Assess the morphology of the erythrocytes.
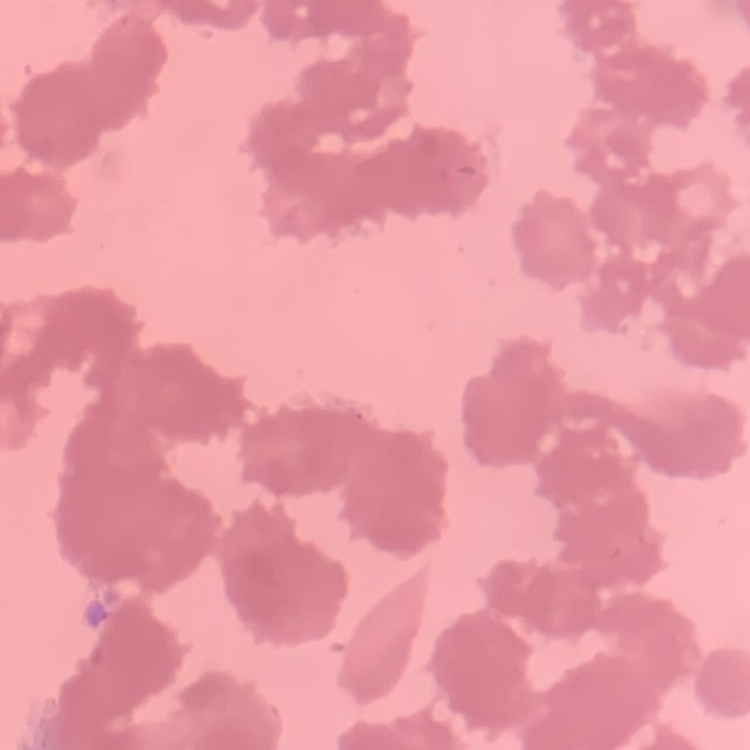
They show rouleaux formation.

One tile cut from a larger photomicrograph. Thin blood smear. Stained with either Field's or Giemsa.